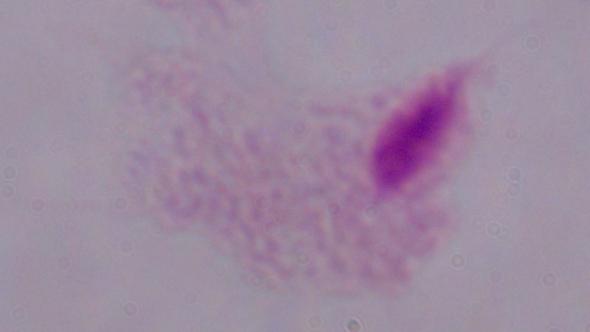

modality = micrograph
magnification = 1000x
identification = trichomonad